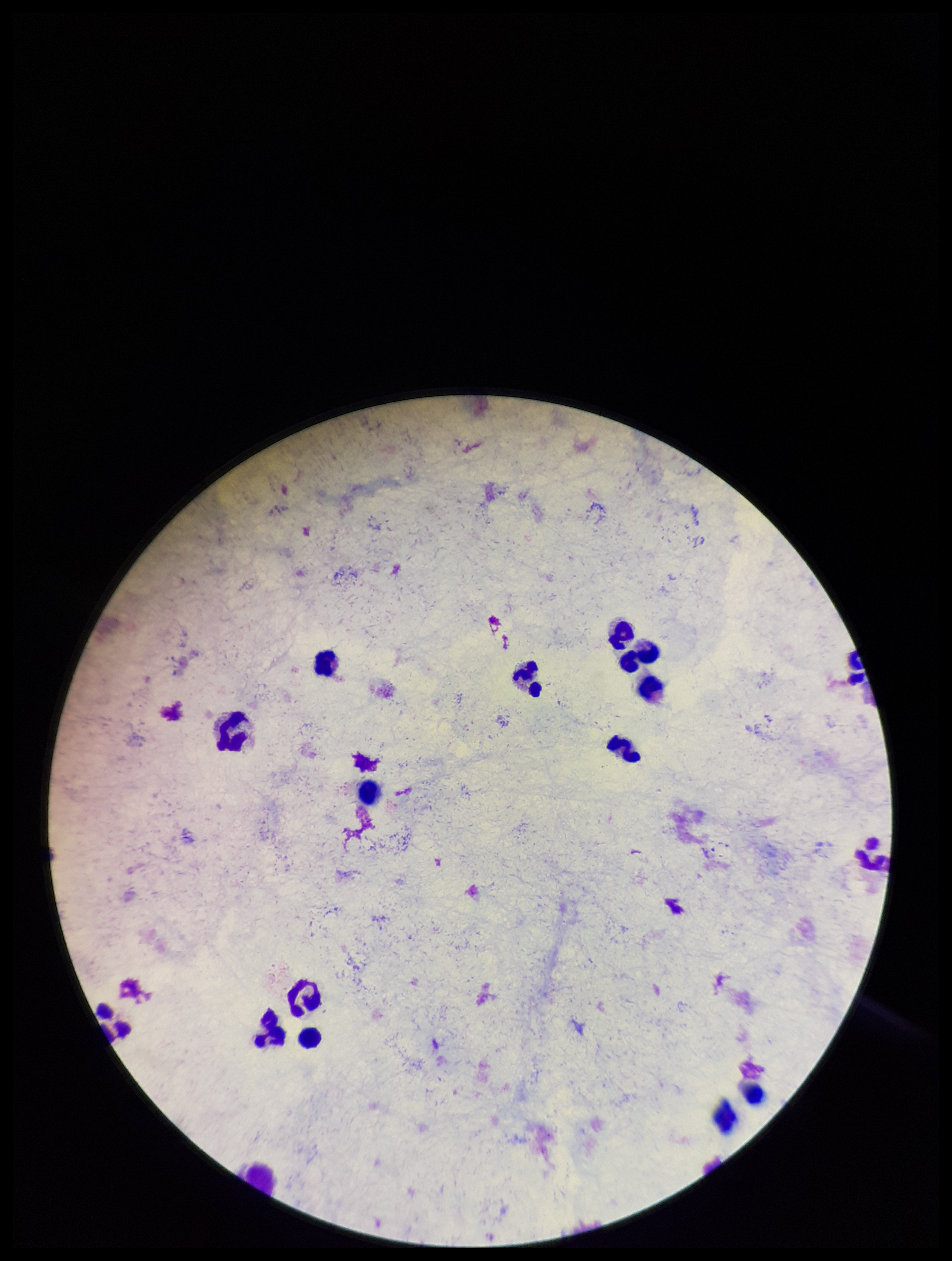

Leukocyte count: 14. Parasite count: 0. Image is 952×1261 pixels. Single field of view. Smartphone photograph taken through the eyepiece of a microscope. Giemsa stain. Preparation: thick. Plasmodium parasites: none seen. Patient malaria status: negative.